Assess the morphology of the red blood cells.
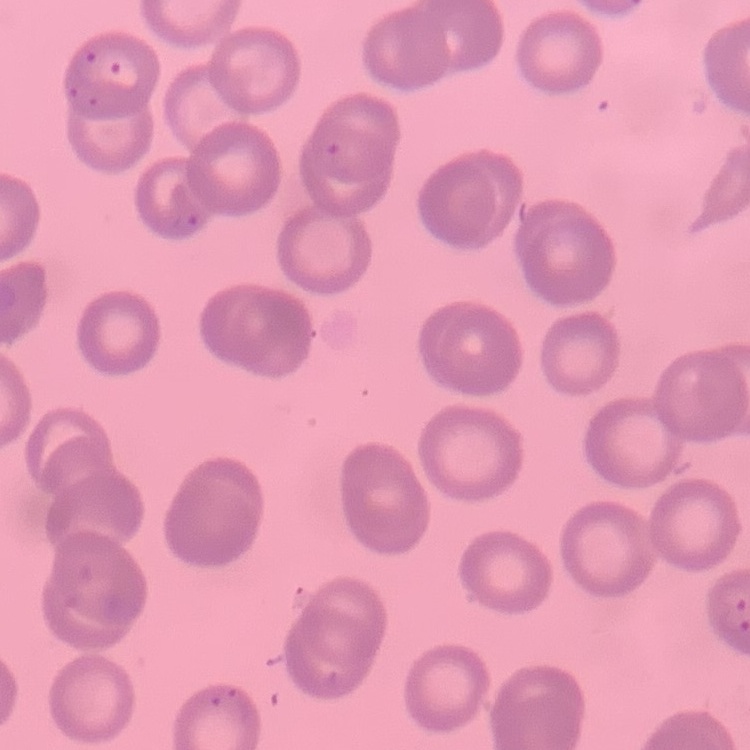

No rouleaux formation.

Thin peripheral smear. Square crop of a larger photomicrograph. Field's or Giemsa stain.